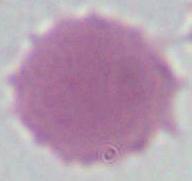
magnification = 1000x
modality = photomicrograph
identification = red blood cell